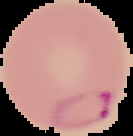

Summary:
  - Malaria status: parasitized
  - Image size: 133×136 pixels
  - Image type: segmented cell region on a black background
  - Preparation: thin blood film